Classify this cell by malaria status.
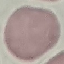
Uninfected.

Automatically extracted cell patch, resized to 64 × 64 pixels. Photographed with a smartphone camera at the microscope eyepiece. Giemsa stain. Thin blood film.